Name the parasite shown.
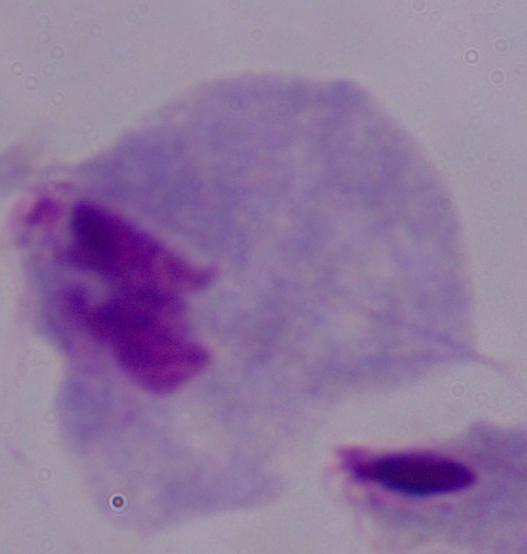

This is a trichomonad.

Photomicrograph. Captured at 1000x magnification.